Identify the parasite.
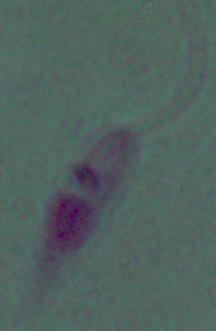

This is Leishmania.

magnification = 1000x
modality = photomicrograph